Give the position of every leukocyte visible.
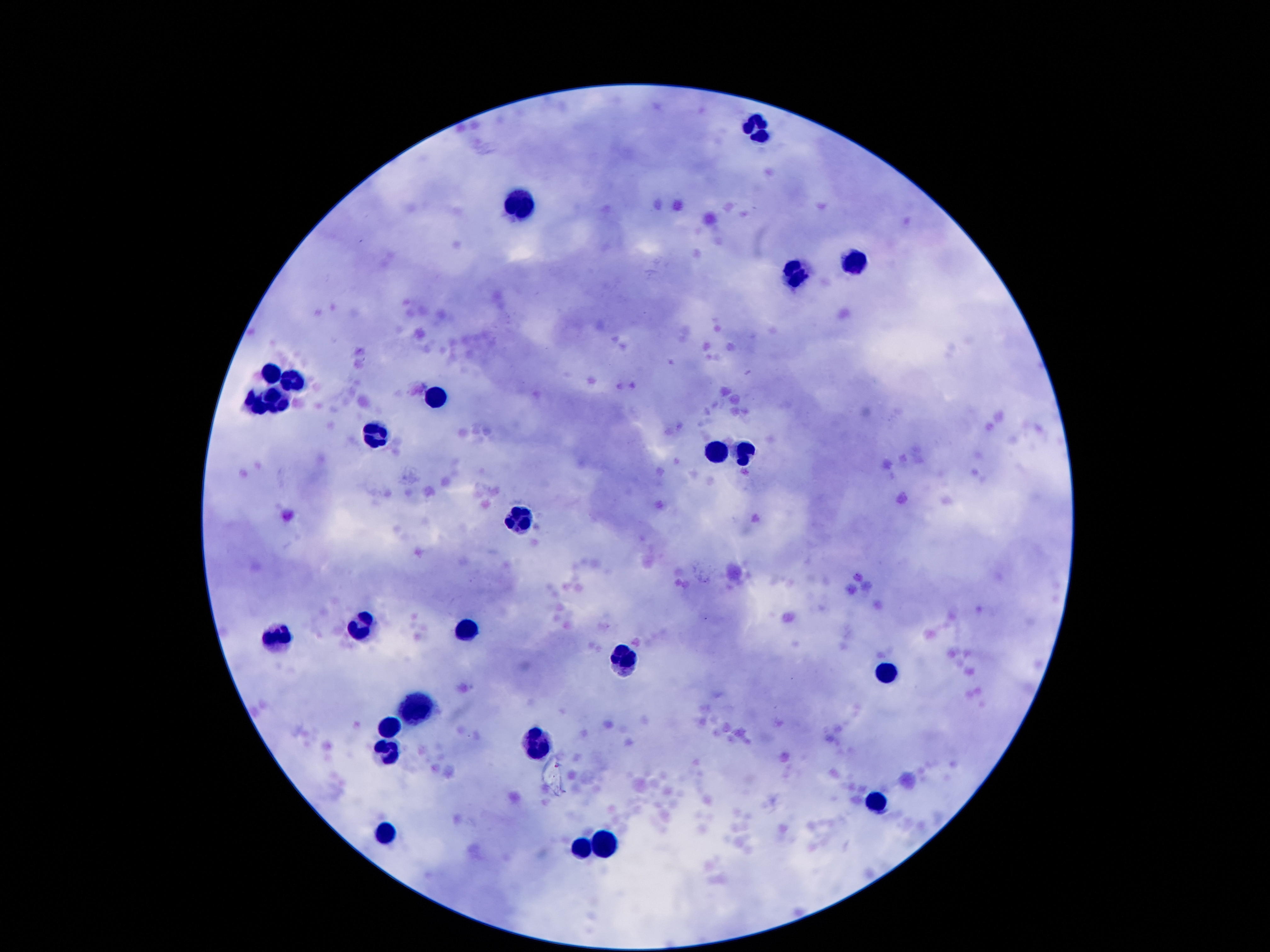
Approximate centers as [x, y] in pixels.
Leukocytes: [758, 125], [520, 207], [853, 261], [796, 273], [268, 373], [299, 382], [438, 393], [279, 402], [257, 404], [374, 432], [747, 450], [717, 454], [518, 516], [361, 627], [465, 629], [282, 638], [628, 656], [887, 672], [418, 706], [390, 727], [545, 742], [388, 754], [878, 801], [390, 834], [601, 840], [581, 847].

field of view = single
image size = 1270×952 pixels
patient malaria status = uninfected
capture = smartphone camera through the microscope eyepiece
preparation = thick blood film
stain = Giemsa
magnification = 100x